Point out every malaria parasite and every leukocyte.
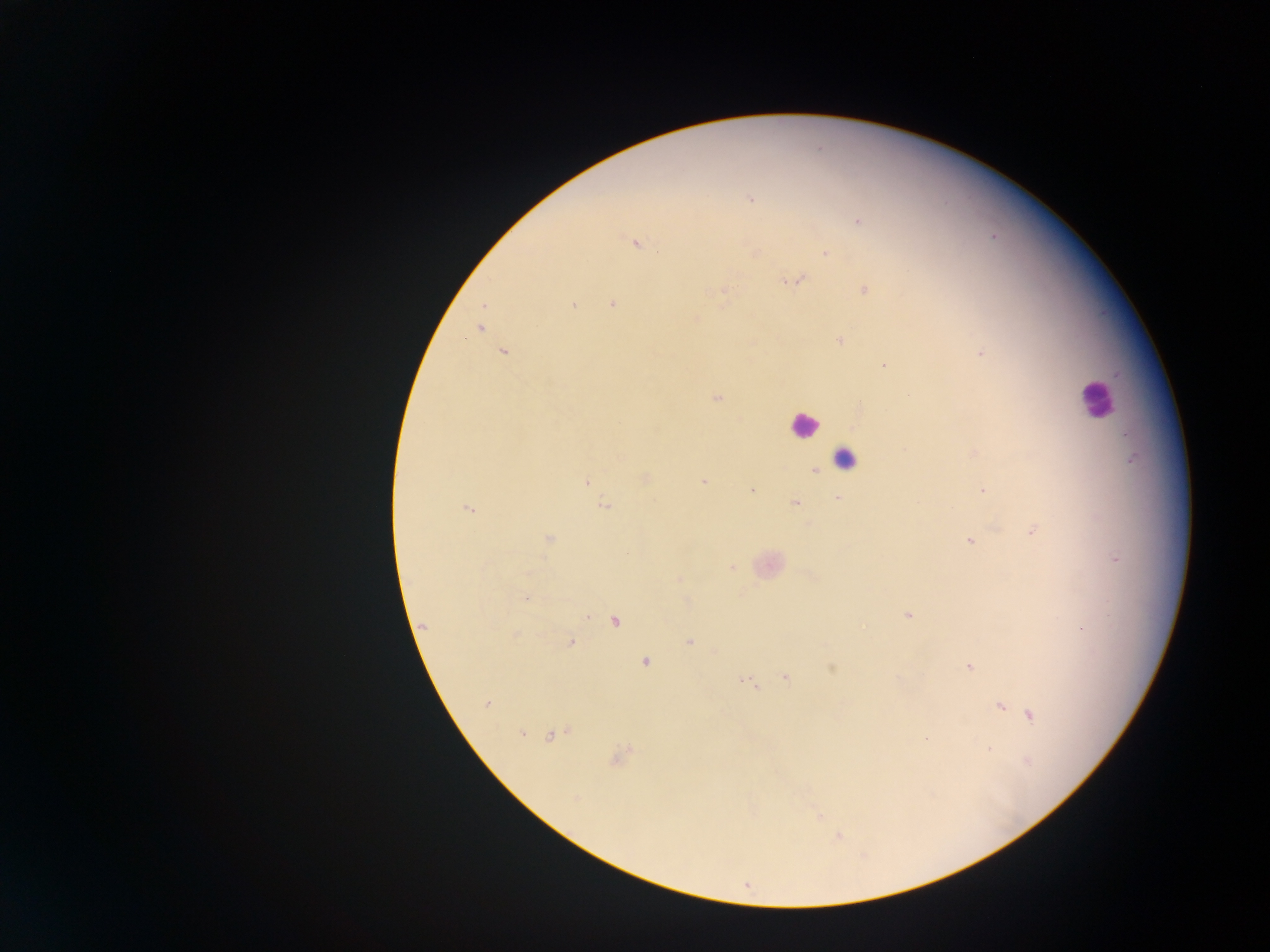

Approximate centers as (x, y) in pixels.
Malaria parasites: (750, 199), (859, 222), (634, 244), (755, 253), (825, 253), (796, 280), (864, 290), (723, 292), (613, 304), (573, 305), (696, 319), (479, 328), (840, 341), (503, 351), (980, 353), (884, 366), (717, 398), (974, 453), (1132, 459), (815, 471), (645, 478), (703, 481), (587, 482), (752, 490), (982, 490), (838, 498), (795, 502), (604, 506), (469, 509), (1032, 531), (548, 540), (969, 541), (1116, 559), (731, 568), (679, 579), (527, 597), (908, 616), (615, 621), (425, 626), (515, 635), (689, 642), (571, 643), (645, 661), (969, 667), (832, 668), (785, 677), (746, 683), (487, 704), (1000, 707), (1030, 715), (521, 733), (553, 735), (927, 738), (988, 748), (617, 756), (1027, 762), (575, 798), (819, 817), (838, 837).
Leukocytes: (1095, 400), (803, 424), (845, 458).

Summary:
  - Field of view: single
  - Capture: mobile-phone photograph through a microscope
  - Country: Ghana
  - Image size: 1270×952 pixels
  - Preparation: thick blood film